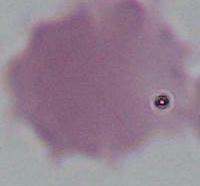

Summary:
  - Identification: red blood cell
  - Magnification: 1000x
  - Modality: micrograph